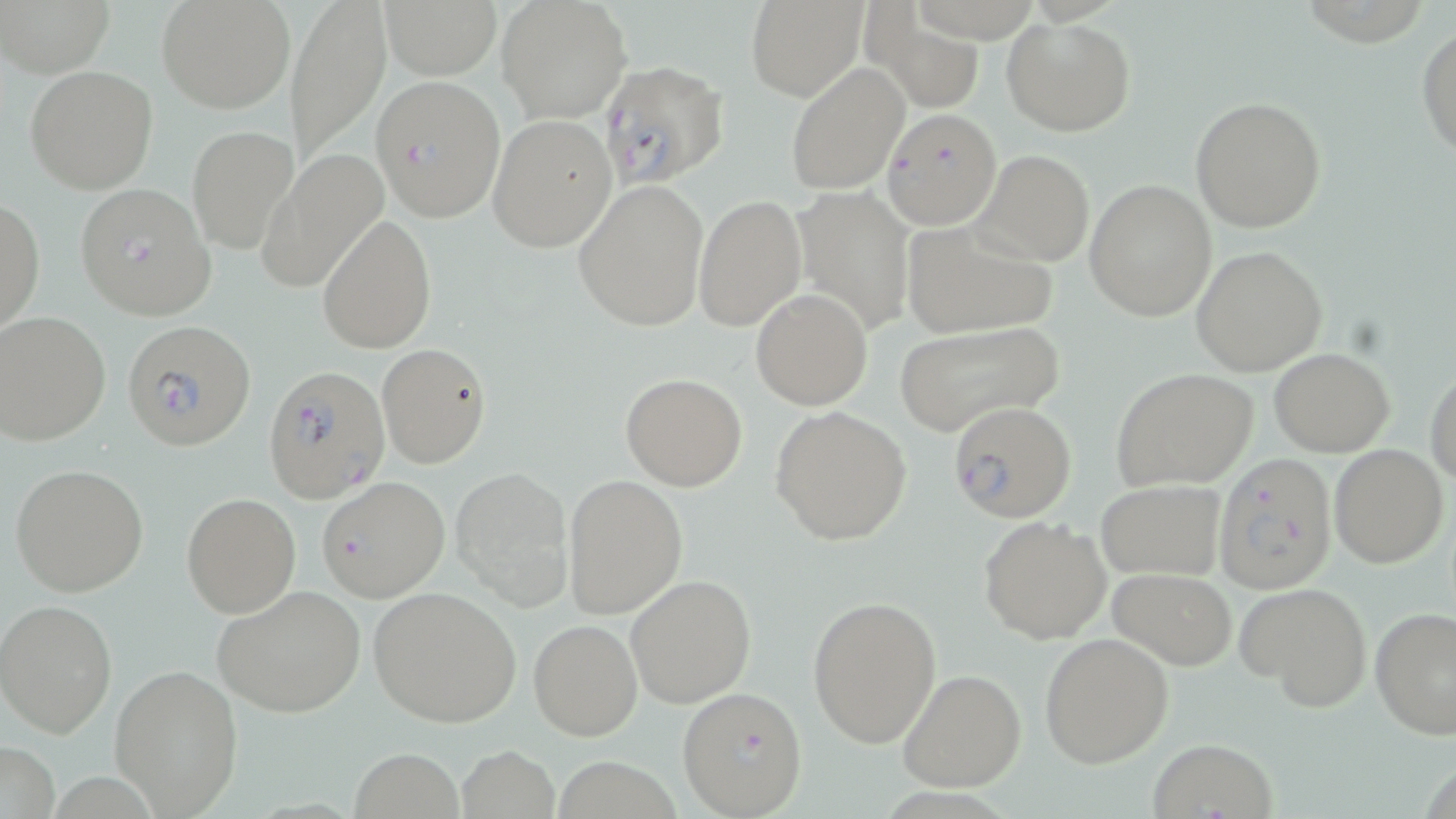
slide-level diagnosis = Plasmodium falciparum
stain = May-Grünwald-Giemsa
uninfected red blood cell locations = approximate bounding boxes as named x1/y1/x2/y2 corners in pixels: (x1=4, y1=0, x2=115, y2=78), (x1=157, y1=0, x2=295, y2=114), (x1=287, y1=0, x2=391, y2=165), (x1=497, y1=0, x2=631, y2=123), (x1=747, y1=0, x2=867, y2=101), (x1=384, y1=3, x2=501, y2=77), (x1=870, y1=13, x2=984, y2=108), (x1=1002, y1=15, x2=1135, y2=137), (x1=1417, y1=24, x2=1456, y2=162), (x1=784, y1=62, x2=909, y2=195), (x1=26, y1=64, x2=159, y2=194), (x1=1193, y1=96, x2=1326, y2=233), (x1=488, y1=113, x2=618, y2=252), (x1=187, y1=125, x2=298, y2=253), (x1=975, y1=148, x2=1095, y2=266), (x1=257, y1=149, x2=387, y2=294), (x1=573, y1=179, x2=709, y2=332), (x1=1084, y1=180, x2=1217, y2=321), (x1=792, y1=186, x2=917, y2=336), (x1=694, y1=195, x2=807, y2=330), (x1=0, y1=198, x2=45, y2=338), (x1=317, y1=214, x2=435, y2=354), (x1=900, y1=220, x2=1058, y2=341), (x1=1191, y1=246, x2=1328, y2=376), (x1=751, y1=290, x2=873, y2=409), (x1=0, y1=310, x2=112, y2=446), (x1=892, y1=320, x2=1065, y2=438), (x1=377, y1=344, x2=491, y2=467), (x1=1269, y1=348, x2=1396, y2=456), (x1=1426, y1=364, x2=1456, y2=488), (x1=1110, y1=367, x2=1260, y2=491), (x1=621, y1=373, x2=748, y2=491), (x1=769, y1=405, x2=913, y2=546), (x1=1329, y1=445, x2=1448, y2=568), (x1=10, y1=463, x2=149, y2=596), (x1=451, y1=465, x2=574, y2=611), (x1=564, y1=474, x2=688, y2=619), (x1=316, y1=476, x2=450, y2=602), (x1=1095, y1=478, x2=1225, y2=581), (x1=181, y1=492, x2=301, y2=617), (x1=978, y1=515, x2=1114, y2=644), (x1=1108, y1=566, x2=1237, y2=669), (x1=625, y1=574, x2=755, y2=708), (x1=1237, y1=581, x2=1373, y2=713), (x1=212, y1=584, x2=367, y2=718), (x1=369, y1=586, x2=522, y2=728), (x1=807, y1=594, x2=942, y2=749), (x1=0, y1=599, x2=118, y2=737), (x1=1370, y1=608, x2=1456, y2=739), (x1=528, y1=619, x2=642, y2=741), (x1=1039, y1=632, x2=1174, y2=768), (x1=108, y1=662, x2=245, y2=817), (x1=897, y1=669, x2=1025, y2=792), (x1=1146, y1=737, x2=1279, y2=818), (x1=1, y1=740, x2=60, y2=819), (x1=455, y1=745, x2=559, y2=819), (x1=351, y1=747, x2=465, y2=818)
preparation = thin blood smear
image size = 1456×819 pixels
field of view = single
magnification = 1000x
Plasmodium falciparum-infected red blood cell locations = approximate bounding boxes as named x1/y1/x2/y2 corners in pixels: (x1=600, y1=60, x2=729, y2=187), (x1=370, y1=74, x2=505, y2=222), (x1=877, y1=110, x2=1004, y2=232), (x1=74, y1=183, x2=216, y2=319), (x1=124, y1=320, x2=256, y2=452), (x1=262, y1=362, x2=388, y2=504), (x1=947, y1=400, x2=1077, y2=522), (x1=1212, y1=454, x2=1337, y2=596), (x1=677, y1=684, x2=807, y2=817)
modality = light microscopy